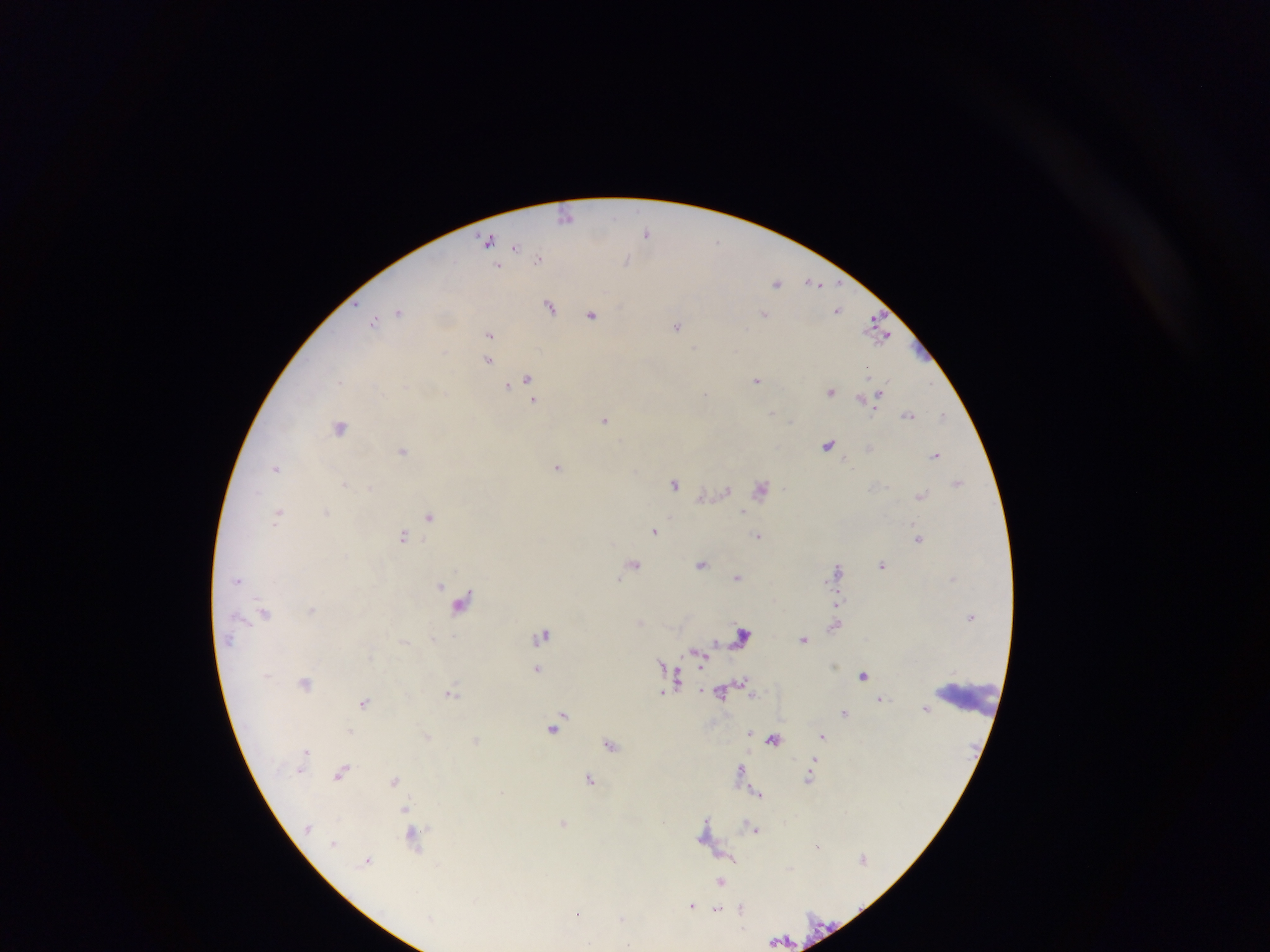
country = Ghana
preparation = thick blood smear
malaria parasite locations = approximate centers as (x, y) in pixels: (566, 216), (646, 233), (488, 239), (716, 242), (516, 246), (539, 257), (627, 261), (497, 266), (813, 282), (777, 283), (550, 306), (838, 310), (399, 311), (764, 313), (592, 314), (374, 320), (677, 326), (746, 328), (876, 329), (489, 334), (695, 347), (443, 350), (488, 360), (528, 378), (757, 380), (340, 382), (507, 386), (830, 392), (444, 393), (706, 393), (533, 400), (771, 413), (908, 415), (943, 415), (605, 419), (791, 421), (341, 427), (828, 445), (870, 448), (403, 451), (935, 455), (557, 466), (277, 468), (674, 483), (958, 483), (345, 484), (370, 487), (727, 489), (761, 489), (920, 496), (326, 511), (743, 512), (279, 514), (430, 516), (654, 530), (403, 536), (758, 536), (918, 538), (634, 563), (701, 564), (883, 565), (837, 569), (737, 577), (238, 580), (440, 585), (462, 602), (836, 604), (312, 610), (265, 613), (640, 621), (834, 626), (542, 635), (742, 635), (804, 639), (229, 641), (715, 641), (699, 657), (662, 662), (537, 668), (864, 675), (677, 678), (743, 681), (305, 682), (662, 692), (721, 692), (451, 693), (753, 695), (882, 698), (364, 701), (926, 710), (844, 713), (562, 716), (555, 726), (350, 731), (749, 733), (428, 736), (823, 736), (773, 739), (476, 740), (611, 744), (306, 751), (740, 769), (342, 771), (590, 778), (809, 778), (394, 780), (758, 793), (405, 809), (706, 821), (563, 822), (754, 828), (414, 839), (333, 844), (817, 845), (368, 860), (721, 881), (691, 905), (703, 907), (718, 909), (742, 910), (578, 914), (622, 918), (627, 946)
field of view = single
leukocyte locations = approximate centers as (x, y) in pixels: (972, 698)
image size = 1270×952 pixels
capture = mobile-phone photograph through a microscope